Report the malaria status of this cell.
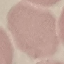

Uninfected.

Summary:
  - Image type: automatically extracted cell patch, resized to 64 × 64 pixels
  - Preparation: thin blood film
  - Stain: Giemsa
  - Capture: smartphone through the microscope eyepiece